Identify the cell.
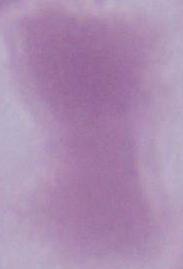
An erythrocyte.

magnification: 1000x
modality: photomicrograph